Locate every Plasmodium falciparum-infected red blood cell.
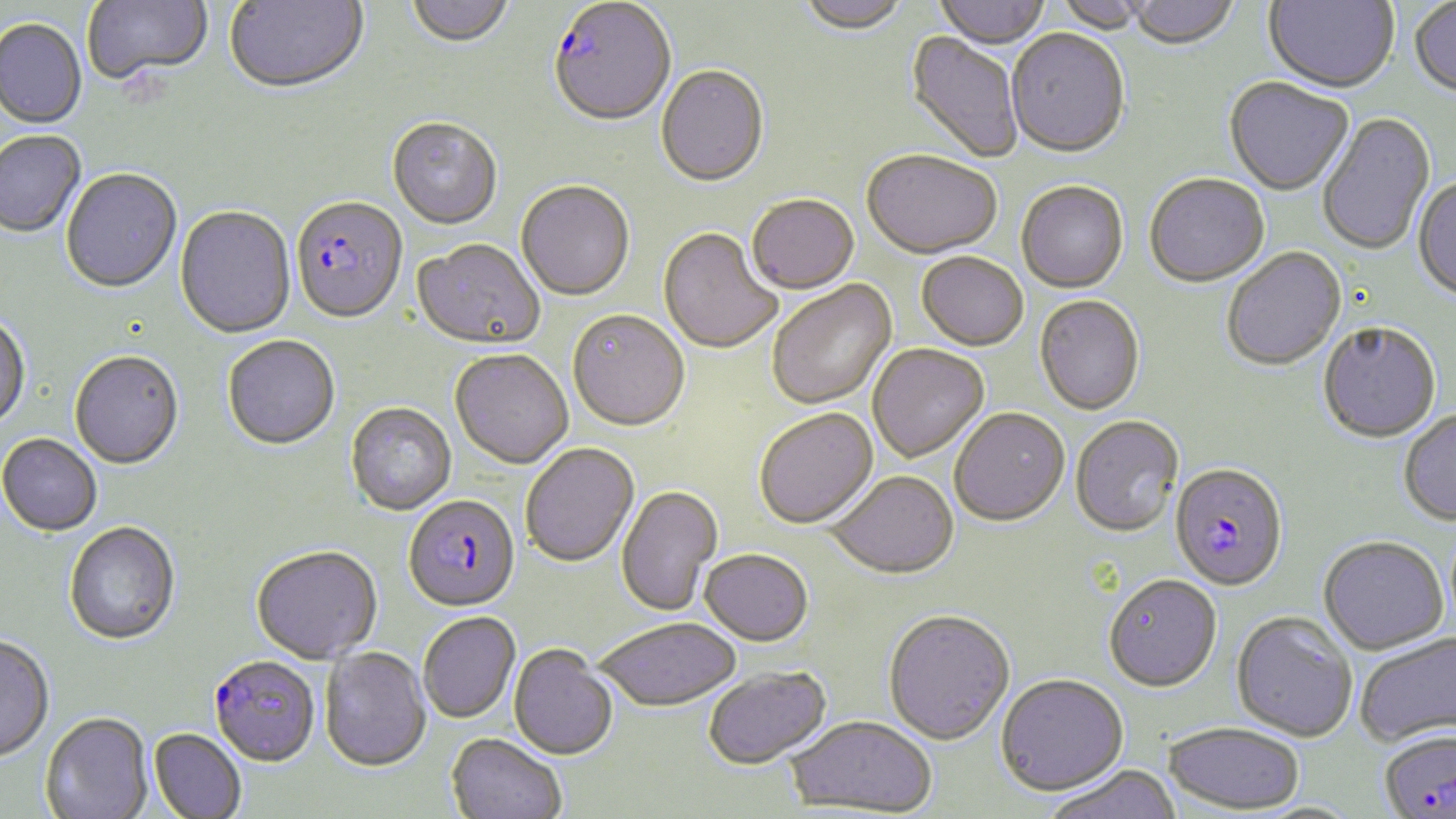

Approximate bounding boxes as [x1, y1, x2, y2] in pixels.
Plasmodium falciparum-infected red blood cells: [548, 2, 676, 130], [290, 199, 409, 326], [1169, 465, 1289, 592], [403, 496, 520, 614], [208, 657, 320, 768].

Summary:
  - Uninfected red blood cell locations: [81, 0, 214, 88], [225, 0, 369, 96], [405, 0, 515, 51], [796, 0, 909, 38], [932, 0, 1051, 52], [1054, 0, 1152, 35], [1128, 0, 1238, 52], [1264, 0, 1399, 96], [1410, 1, 1456, 100], [0, 20, 86, 130], [904, 31, 1023, 164], [1006, 31, 1130, 161], [656, 66, 770, 190], [1224, 79, 1354, 197], [1317, 113, 1436, 258], [387, 119, 503, 232], [0, 132, 86, 239], [862, 152, 1002, 262], [61, 170, 182, 295], [1144, 176, 1270, 290], [1412, 176, 1456, 304], [516, 182, 635, 303], [1016, 183, 1129, 294], [747, 197, 860, 296], [175, 206, 296, 339], [658, 230, 781, 356], [411, 240, 545, 353], [1222, 249, 1347, 373], [916, 255, 1028, 353], [768, 281, 898, 410], [1034, 297, 1145, 417], [568, 312, 690, 434], [0, 315, 31, 432], [1318, 324, 1441, 445], [223, 336, 340, 452], [867, 344, 989, 464], [449, 351, 573, 471], [69, 352, 184, 471], [345, 404, 457, 517], [754, 409, 879, 530], [950, 410, 1070, 529], [1399, 410, 1456, 526], [1070, 417, 1185, 539], [0, 434, 102, 537], [520, 444, 640, 568], [825, 472, 959, 582], [616, 486, 723, 617], [63, 522, 180, 646], [1319, 536, 1450, 655], [251, 547, 382, 665], [699, 551, 813, 649], [1103, 576, 1222, 694], [883, 612, 1015, 747], [1231, 612, 1358, 742], [417, 613, 521, 724], [597, 620, 742, 714], [1355, 631, 1456, 749], [0, 634, 55, 761], [509, 645, 617, 762], [319, 648, 431, 773], [703, 667, 832, 771], [995, 674, 1129, 798], [40, 713, 153, 819], [786, 717, 938, 815], [1162, 721, 1304, 815], [1378, 727, 1456, 818], [148, 728, 246, 817], [446, 734, 566, 819], [1045, 765, 1182, 819]
  - Slide-level diagnosis: Plasmodium falciparum
  - Image size: 1456×819 pixels
  - Stain: May-Grünwald-Giemsa
  - Field of view: single
  - Magnification: 1000x
  - Preparation: thin blood smear
  - Modality: light microscopy